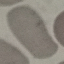
Summary:
  - Result: negative for malaria parasites
  - Preparation: thin blood film
  - Stain: Giemsa
  - Image type: cell patch, automatically extracted from a larger field of view and resized to 64 × 64 pixels
  - Capture: smartphone camera at the microscope eyepiece